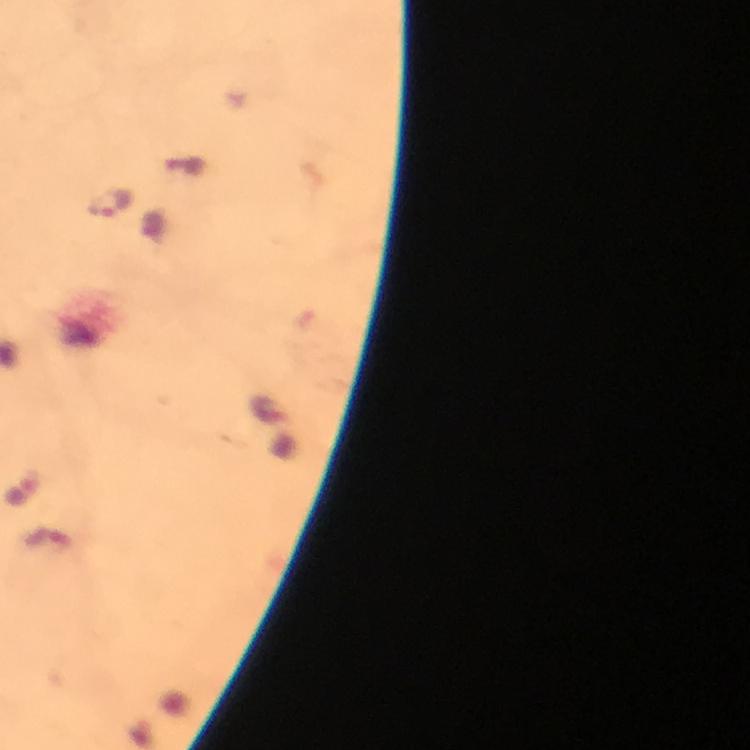
image size = 750×750 pixels
magnification = 100x
stain = Giemsa
capture = smartphone camera through the microscope
preparation = thick smear
immersion oil = applied
context = from a diagnostic examination for malaria
cropped from = a single field of view
Plasmodium parasite locations = approximate object centers, in pixels from the top-left corner: (x=110, y=203), (x=22, y=494)